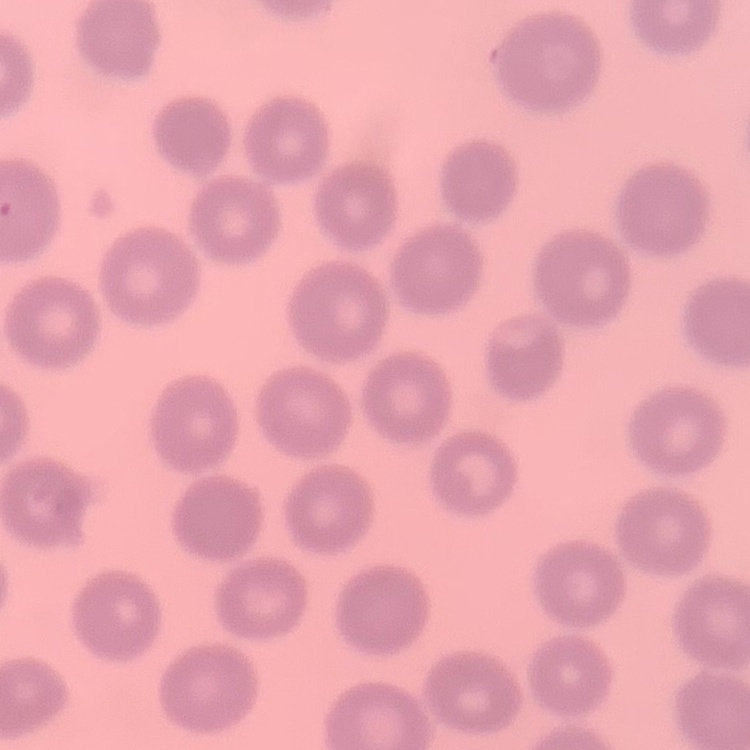

The red blood cells exhibit no rouleaux formation. Thin blood film. Square crop of a larger photomicrograph. Field's or Giemsa stain.